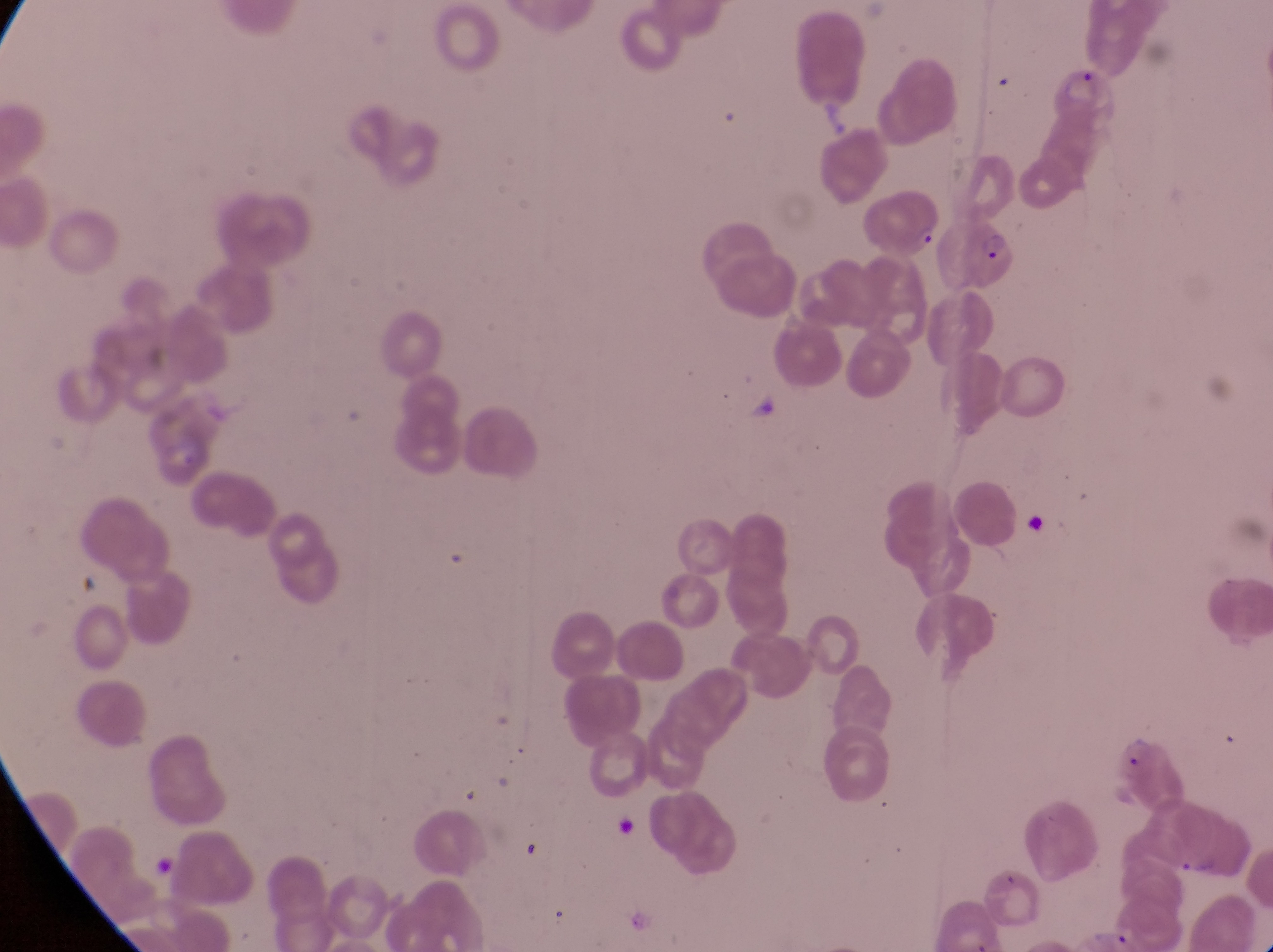

Approximate bounding boxes as left top right bottom in pixels. Artifact (platelet-like body, stain precipitate, or debris) locations: 739 387 797 450; 1025 507 1052 542. Parasitised red blood cell locations: 852 185 944 257; 958 204 1025 291. Photographed through the eyepiece of an Olympus CX-23 microscope with a smartphone camera. Thin blood smear. Sample from Uganda. Magnification of 1000x. Single field of view. Image is 1273×952 pixels.